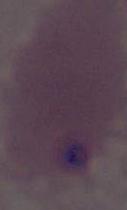
identification: red blood cell
magnification: 1000x
modality: photomicrograph